Comment on the morphology of the erythrocytes.
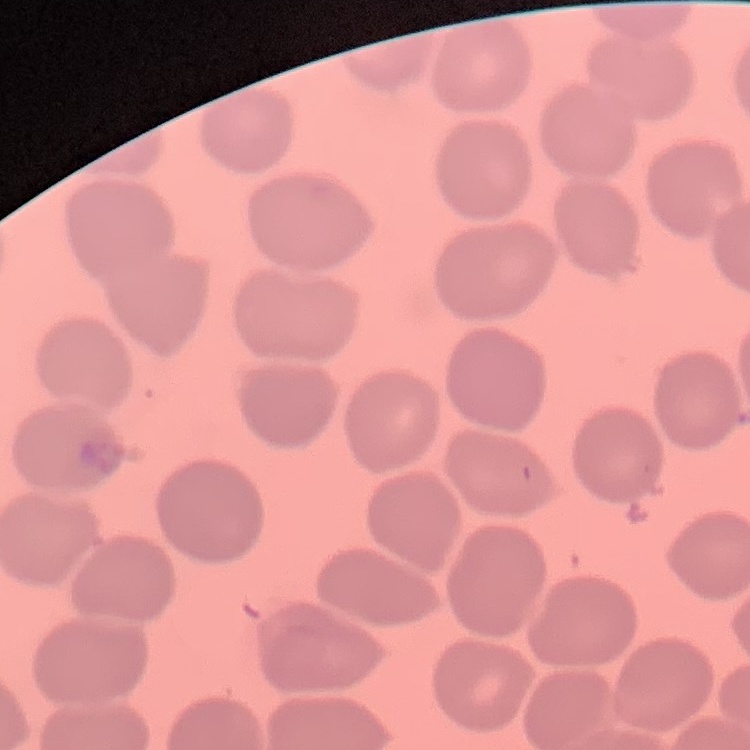
No rouleaux formation.

preparation: thin blood film
image_type: square crop of a larger photomicrograph
stain: Field's or Giemsa